Name the parasite shown.
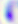

Toxoplasma gondii.

Summary:
  - Magnification: 400x
  - Modality: photomicrograph